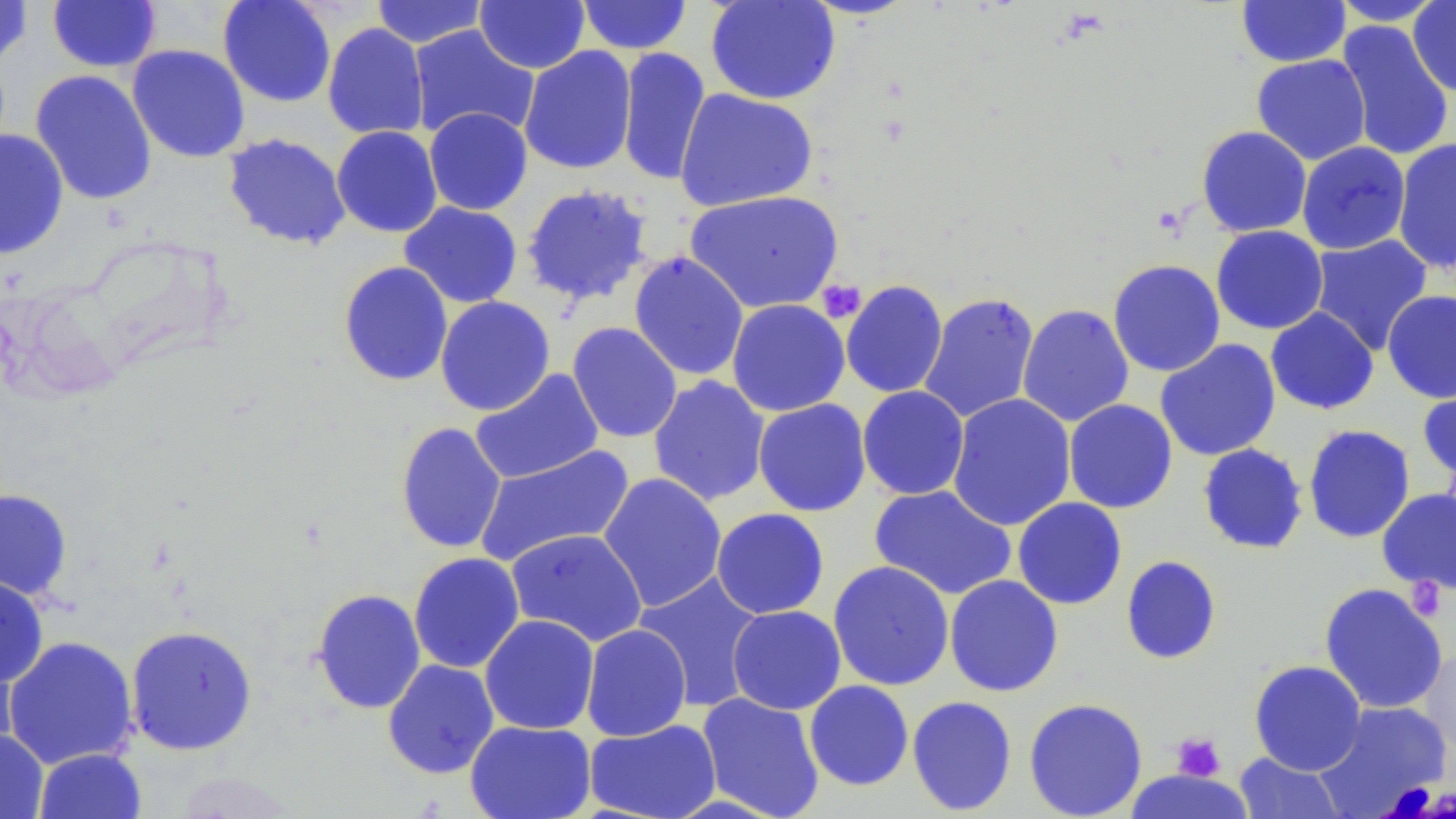

Approximate bounding boxes as (x1, y1, x2, y2) in pixels. Platelet locations: (816, 279, 866, 324), (1406, 578, 1447, 621), (1171, 732, 1225, 781). Uninfected red blood cell locations: (0, 0, 33, 70), (47, 0, 162, 73), (217, 0, 337, 108), (370, 0, 489, 48), (475, 0, 590, 73), (577, 0, 692, 55), (705, 0, 841, 105), (1236, 0, 1351, 67), (1329, 0, 1447, 26), (1408, 1, 1456, 98), (1335, 20, 1454, 162), (322, 22, 430, 140), (408, 24, 540, 143), (127, 44, 251, 162), (518, 46, 637, 175), (616, 48, 711, 187), (1251, 54, 1371, 165), (30, 69, 157, 206), (674, 88, 819, 212), (424, 107, 533, 215), (331, 125, 443, 237), (1196, 126, 1312, 237), (0, 128, 69, 259), (222, 133, 352, 251), (1392, 138, 1456, 274), (1296, 142, 1411, 255), (520, 183, 654, 307), (683, 190, 844, 314), (399, 201, 523, 308), (1211, 225, 1329, 334), (1308, 234, 1434, 355), (628, 252, 749, 381), (1108, 259, 1226, 377), (337, 260, 453, 386), (840, 280, 949, 399), (1382, 290, 1456, 403), (918, 292, 1039, 423), (434, 296, 555, 416), (726, 299, 850, 417), (1017, 304, 1135, 427), (1265, 307, 1379, 415), (567, 322, 683, 443), (1155, 339, 1281, 461), (470, 368, 604, 484), (648, 375, 770, 506), (1417, 382, 1456, 484), (857, 385, 970, 500), (947, 393, 1076, 532), (753, 399, 871, 516), (1063, 399, 1178, 514), (395, 421, 507, 554), (1302, 424, 1416, 543), (1197, 443, 1309, 555), (474, 444, 636, 567), (598, 472, 727, 612), (868, 484, 1017, 600), (0, 488, 73, 600), (1377, 488, 1456, 594), (1012, 497, 1127, 610), (711, 508, 829, 619), (506, 528, 647, 647), (408, 552, 525, 674), (1120, 555, 1222, 665), (828, 561, 954, 691), (633, 572, 766, 711), (944, 574, 1064, 697), (0, 575, 49, 688), (1319, 583, 1449, 714), (311, 588, 427, 714), (727, 605, 846, 715), (480, 614, 599, 735), (580, 624, 691, 741), (124, 625, 258, 756), (1, 635, 139, 770), (0, 638, 21, 759), (1418, 643, 1456, 757), (382, 659, 500, 779), (1249, 660, 1366, 775), (804, 680, 914, 791), (696, 692, 826, 819), (907, 695, 1018, 816), (1023, 698, 1148, 818), (1314, 701, 1453, 814), (584, 718, 721, 819), (465, 720, 596, 819), (0, 728, 49, 819), (33, 747, 147, 819), (1234, 752, 1347, 819). Slide-level diagnosis: negative for blood parasites. Thin blood smear. Light microscopy. May-Grünwald-Giemsa-stained preparation. Captured at 1000x magnification. Image is 1456×819 pixels. Single field of view.